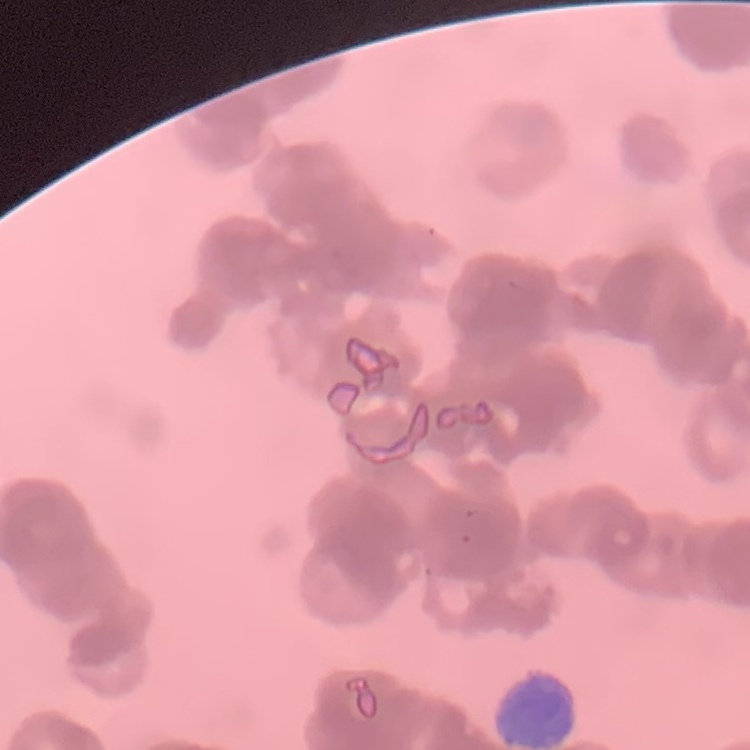
The erythrocytes show rouleaux formation. Field's or Giemsa stain. Thin blood smear. One tile cut from a larger photomicrograph.